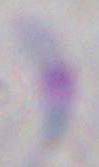
Summary:
  - Identification: Toxoplasma gondii
  - Modality: micrograph
  - Magnification: 1000x